Locate every leukocyte (white blood cell).
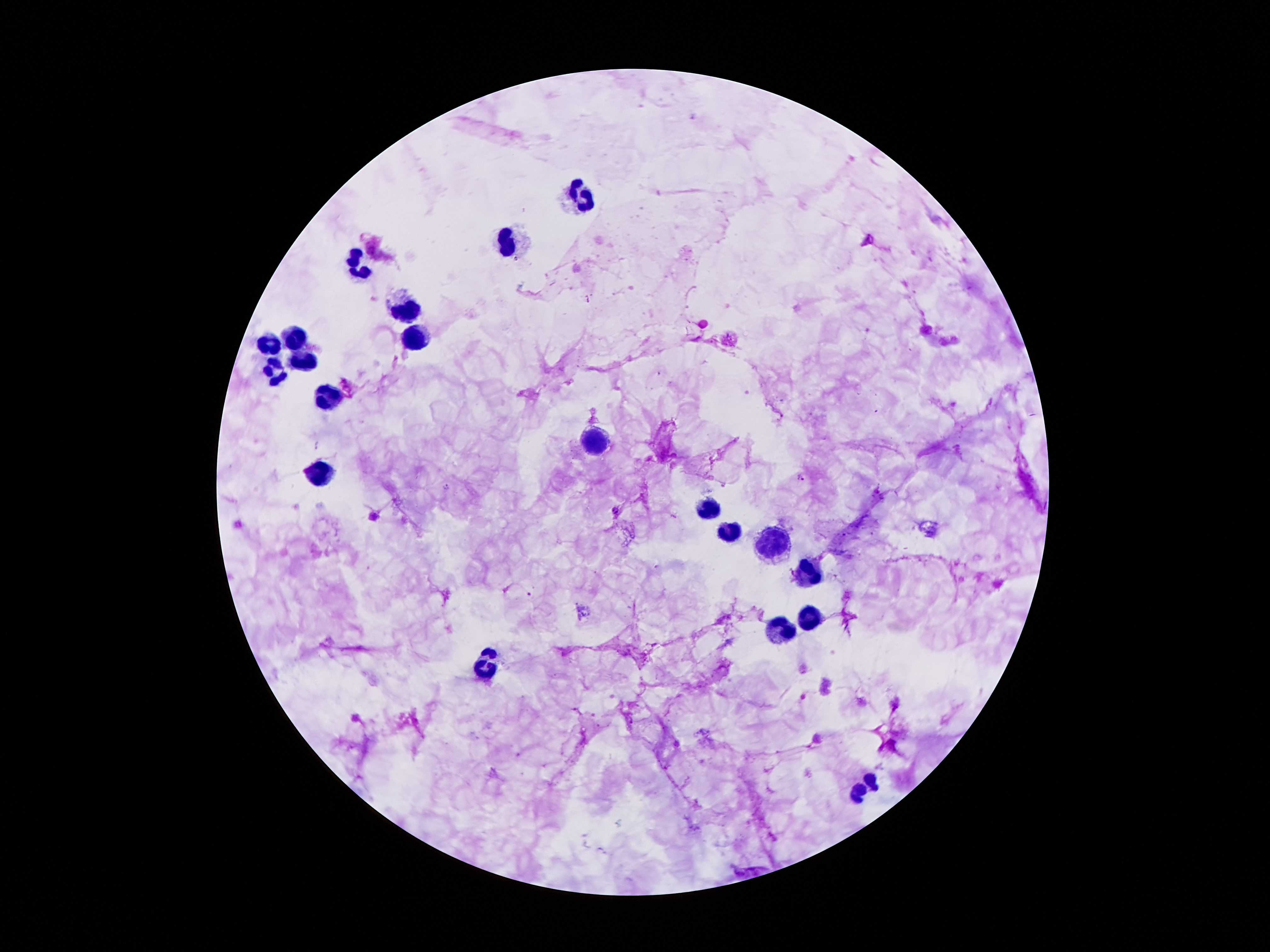

Approximate object centers, in pixels from the top-left corner.
Leukocytes: (x=575, y=196), (x=505, y=244), (x=355, y=266), (x=403, y=314), (x=413, y=337), (x=295, y=338), (x=269, y=345), (x=302, y=362), (x=277, y=373), (x=323, y=397), (x=593, y=444), (x=323, y=473), (x=701, y=505), (x=727, y=532), (x=773, y=540), (x=806, y=573), (x=808, y=617), (x=778, y=632), (x=487, y=665), (x=865, y=786).

Malaria parasite locations: (x=318, y=445), (x=798, y=478), (x=445, y=486). 100x magnification. Patient malaria status: infected with Plasmodium falciparum. Thick blood smear. Image is 1270×952 pixels. Single field of view. Photographed through the microscope eyepiece with a smartphone camera. Giemsa stain.